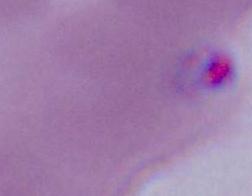
Summary:
  - Identification: erythrocyte
  - Magnification: 1000x
  - Modality: photomicrograph